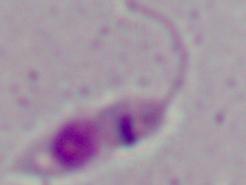

magnification: 1000x
identification: Leishmania
modality: photomicrograph